Assess the morphology of the red blood cells.
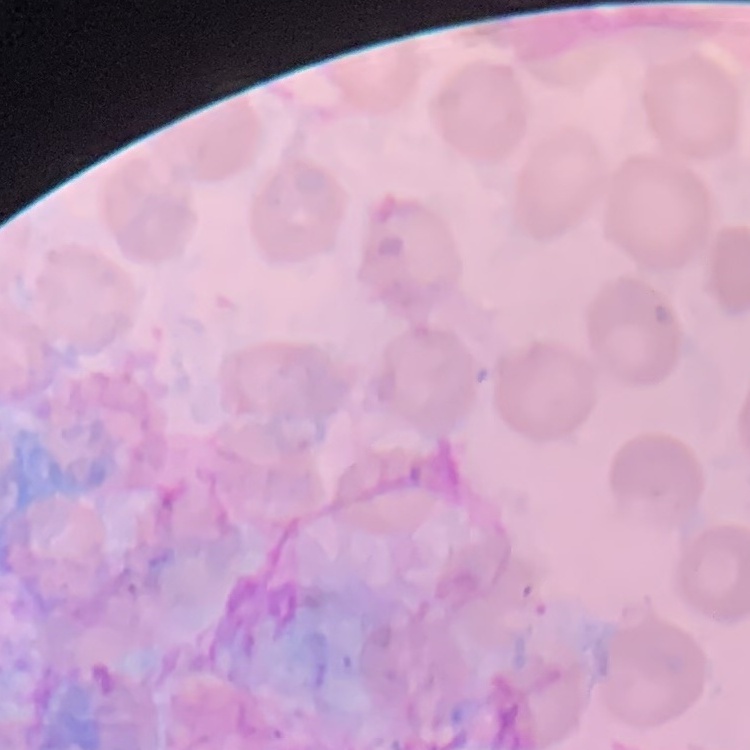
No rouleaux formation.

Summary:
  - Preparation: thin blood smear
  - Stain: Field's or Giemsa
  - Image type: one tile cut from a larger photomicrograph